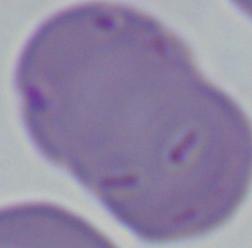
A Babesia parasite is shown. Captured at 1000x magnification. Micrograph.